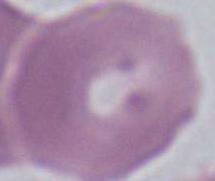

{
  "magnification": "1000x",
  "identification": "red blood cell",
  "modality": "photomicrograph"
}